Assess this cell for malaria.
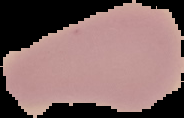

Uninfected.

{
  "image_type": "segmented cell region with the area outside set to black",
  "image_size": "184×118 pixels",
  "preparation": "thin blood film"
}